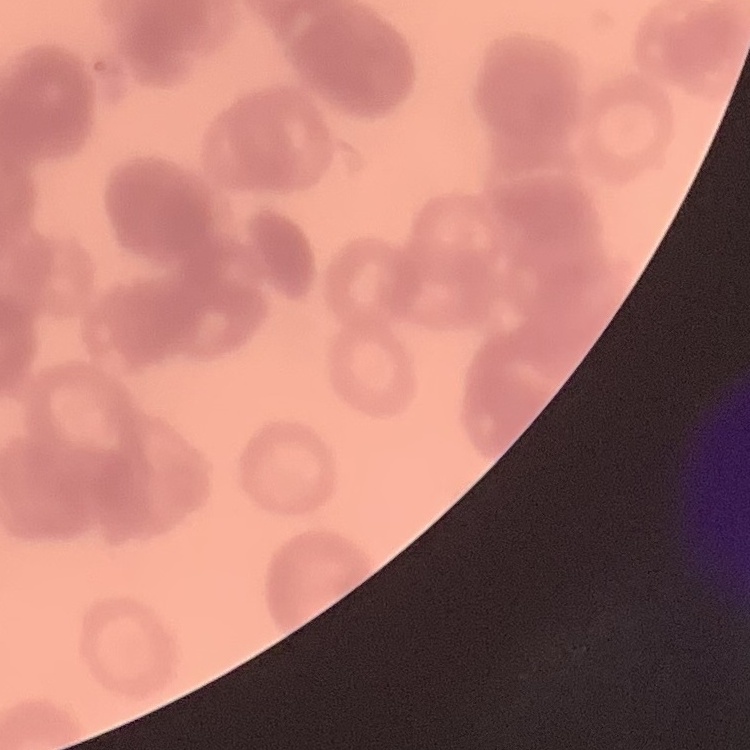
Summary:
  - Erythrocyte morphology: rouleaux formation
  - Image type: square crop of a larger photomicrograph
  - Stain: Field's or Giemsa
  - Preparation: thin blood film